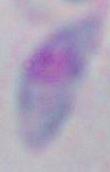

1000x magnification. Photomicrograph. Toxoplasma gondii is shown.